State the blood parasite species.
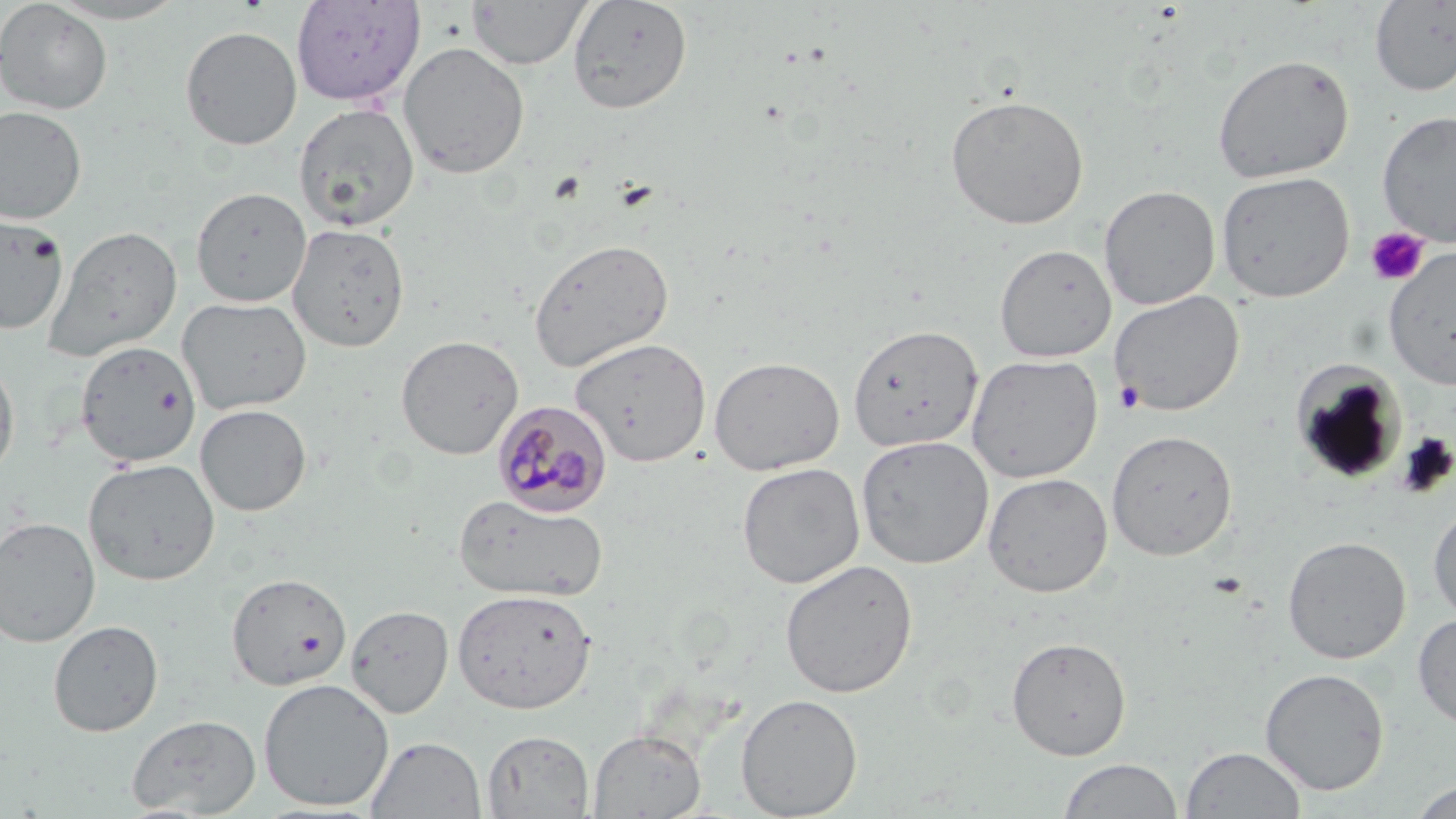
Plasmodium malariae.

Summary:
  - Coordinate format: approximate bounding boxes as (x1,y1)-(x2,y2) corner pairs in pixels
  - Uninfected red blood cell locations: (0,0)-(113,114), (45,0)-(189,24), (290,0)-(425,107), (567,0)-(693,114), (466,1)-(591,70), (1369,1)-(1456,97), (179,25)-(303,150), (397,42)-(530,179), (1212,53)-(1354,183), (944,93)-(1090,230), (293,102)-(420,232), (0,105)-(88,225), (1377,109)-(1456,248), (1215,170)-(1355,303), (1099,185)-(1221,310), (191,186)-(312,307), (0,212)-(69,335), (287,222)-(410,352), (45,226)-(184,362), (528,238)-(674,372), (994,244)-(1116,363), (1384,246)-(1456,391), (1109,290)-(1244,416), (178,295)-(312,415), (847,323)-(983,453), (396,334)-(523,460), (569,337)-(711,468), (76,340)-(202,467), (966,353)-(1103,483), (709,355)-(844,476), (0,357)-(20,480), (1290,363)-(1407,485), (194,404)-(311,516), (1106,429)-(1238,561), (855,435)-(994,568), (83,458)-(221,586), (736,461)-(865,589), (983,472)-(1112,597), (454,493)-(608,603), (1428,500)-(1456,625), (0,516)-(101,647), (1282,535)-(1411,664), (779,558)-(918,698), (226,572)-(351,691), (452,588)-(597,714), (346,604)-(454,718), (1413,614)-(1456,731), (49,620)-(164,737), (1006,636)-(1131,760), (1259,667)-(1390,796), (258,678)-(395,811), (735,694)-(862,818), (126,714)-(262,817), (587,728)-(706,818), (482,730)-(594,818), (366,736)-(486,818), (1181,746)-(1306,819), (1058,758)-(1183,818), (1410,780)-(1455,819)
  - Platelet locations: (614,179)-(659,213), (1364,227)-(1430,287), (1115,380)-(1145,414)
  - Plasmodium malariae-infected red blood cell locations: (492,401)-(613,518)
  - Image size: 1456×819 pixels
  - Modality: light microscopy
  - Magnification: 1000x
  - Field of view: one of a larger specimen
  - Preparation: thin blood smear
  - Stain: May-Grünwald-Giemsa